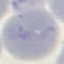 Result: no malaria parasites seen. Cell patch, automatically extracted from a larger field of view and resized to 64 × 64 pixels. Photographed with a smartphone camera at the microscope eyepiece. Giemsa stain. Thin smear of blood.